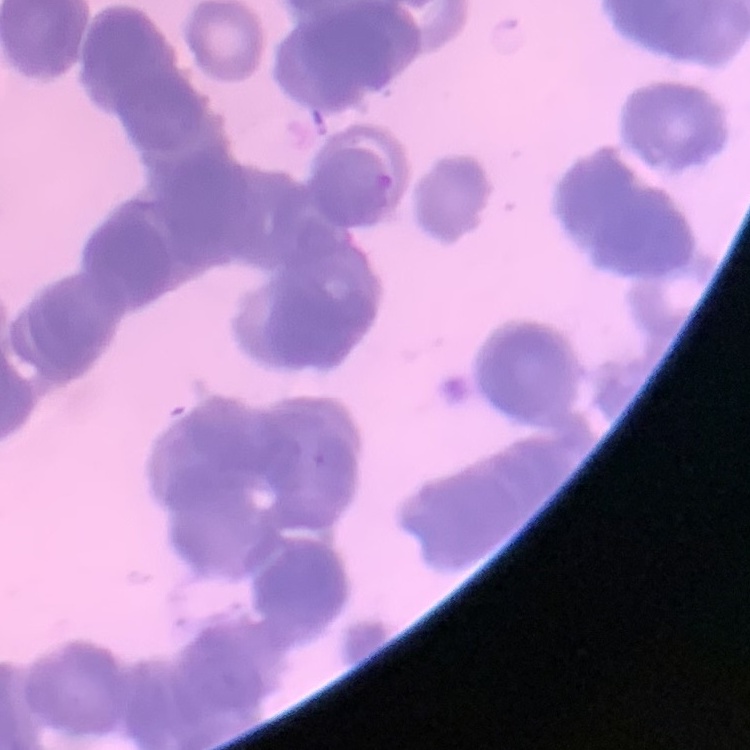

Summary:
  - Red blood cell morphology: rouleaux formation
  - Image type: square crop of a larger photomicrograph
  - Stain: Field's or Giemsa
  - Preparation: thin peripheral smear